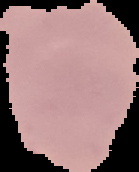

The area outside the segmented cell region is set to black. From a thin blood film. Image is 139×172 pixels. Malaria status: uninfected.